Assess this cell for malaria.
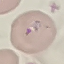
It is parasitized.

stain: Giemsa
image_type: automatically extracted cell patch, resized to 64 × 64 pixels
preparation: thin blood film
capture: smartphone through the microscope eyepiece